Comment on the morphology of the erythrocytes.
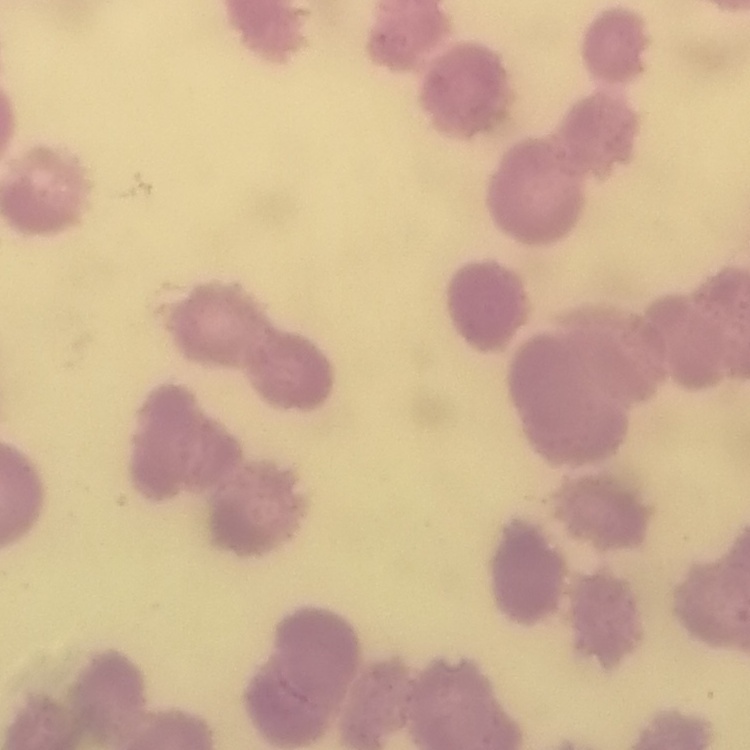

They show rouleaux formation.

image type = one tile cut from a larger photomicrograph
preparation = thin peripheral smear
stain = Field's or Giemsa